Report the malaria status of this cell.
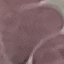

It is uninfected.

Thin blood film. Automatically extracted cell patch, resized to 64 × 64 pixels. Giemsa stain. Photographed with a smartphone camera at the microscope eyepiece.